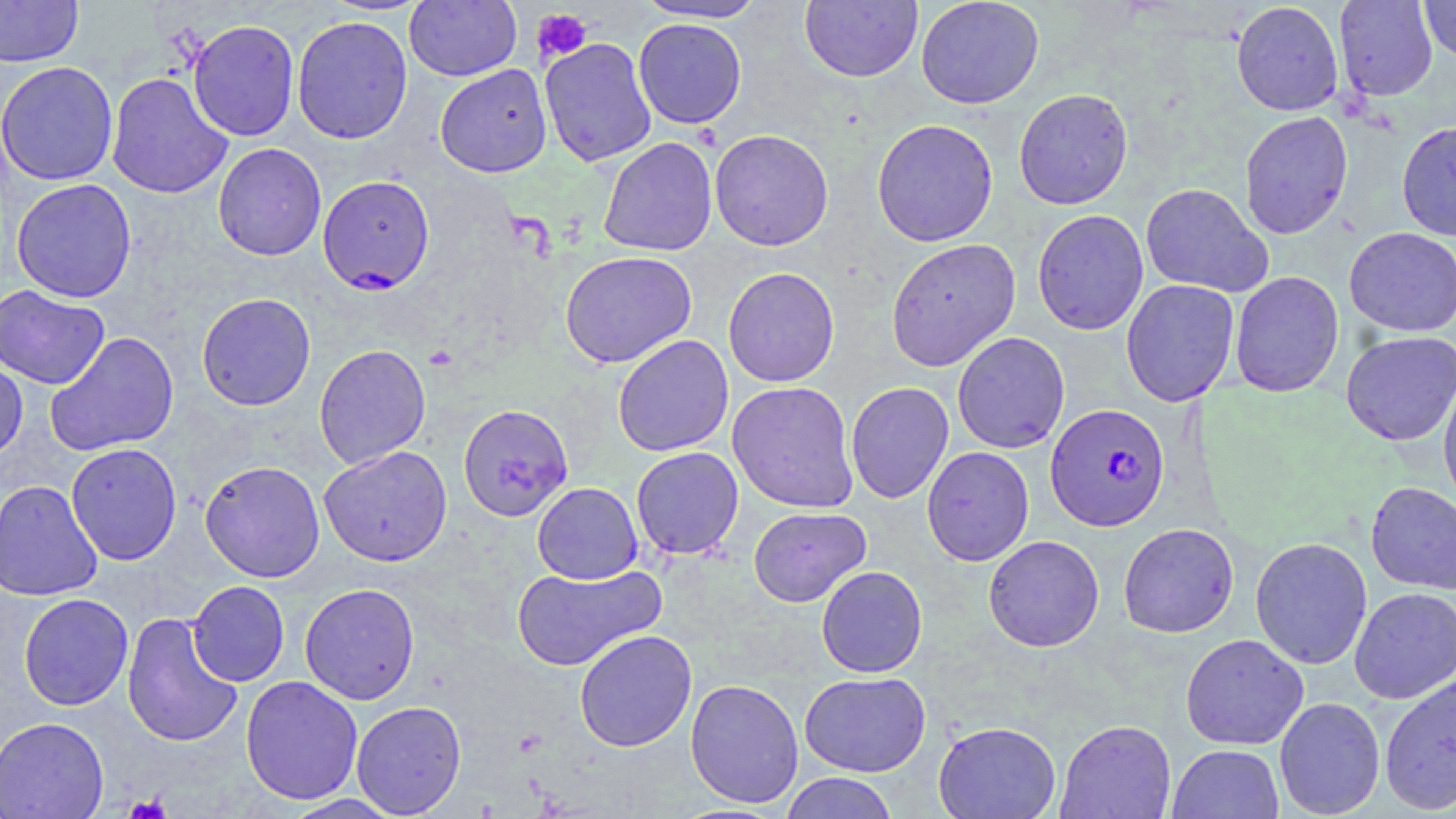

Approximate bounding boxes as (x1, y1, x2, y2) in pixels. Uninfected red blood cell locations: (0, 0, 83, 67), (404, 0, 522, 81), (633, 0, 768, 23), (800, 0, 923, 82), (916, 0, 1044, 109), (1334, 0, 1438, 101), (1419, 0, 1456, 63), (1230, 2, 1344, 116), (292, 15, 413, 144), (633, 18, 747, 129), (187, 19, 300, 141), (539, 37, 657, 167), (0, 61, 119, 187), (435, 64, 552, 177), (106, 72, 233, 200), (1013, 88, 1133, 209), (1239, 110, 1353, 239), (871, 118, 999, 247), (1396, 119, 1456, 241), (709, 129, 834, 251), (597, 137, 717, 257), (212, 143, 326, 261), (11, 178, 137, 303), (1140, 183, 1273, 298), (1032, 209, 1149, 335), (1344, 227, 1456, 337), (885, 238, 1021, 371), (559, 250, 697, 368), (722, 267, 840, 387), (1229, 271, 1344, 397), (1120, 279, 1239, 407), (0, 284, 110, 389), (196, 292, 316, 411), (45, 331, 180, 457), (952, 331, 1070, 453), (1341, 331, 1456, 446), (612, 334, 734, 457), (314, 343, 431, 470), (0, 356, 28, 462), (1438, 374, 1456, 513), (727, 381, 859, 513), (845, 382, 954, 503), (458, 404, 574, 522), (65, 443, 182, 565), (318, 445, 452, 566), (921, 446, 1034, 566), (631, 447, 744, 560), (199, 460, 325, 582), (0, 480, 103, 601), (532, 481, 643, 584), (1365, 481, 1456, 595), (748, 506, 871, 607), (1118, 522, 1239, 638), (983, 535, 1105, 652), (1250, 537, 1373, 669), (511, 563, 666, 672), (816, 565, 927, 678), (187, 581, 290, 686), (299, 583, 420, 704), (1349, 587, 1456, 704), (18, 593, 134, 710), (122, 612, 244, 747), (574, 630, 697, 752), (1180, 633, 1309, 749), (799, 671, 931, 777), (1379, 672, 1456, 814), (240, 675, 363, 805), (685, 678, 803, 808), (1274, 697, 1385, 818), (351, 700, 467, 817), (0, 716, 109, 819), (1056, 719, 1176, 818), (933, 720, 1061, 819), (1168, 744, 1284, 819), (779, 772, 900, 819), (283, 795, 404, 819). Plasmodium falciparum-infected red blood cell locations: (317, 175, 435, 294), (1045, 403, 1170, 531). Platelet locations: (532, 8, 593, 62), (125, 793, 172, 819). Slide-level diagnosis: Plasmodium falciparum. May-Grünwald-Giemsa-stained preparation. Optical microscopy. Image is 1456×819 pixels. Captured at 1000x magnification. Single field of view. Thin blood smear.